State which parasite is depicted.
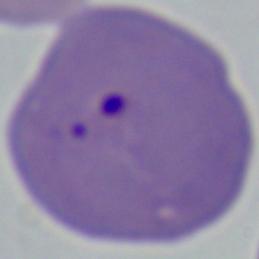

Babesia.

modality = micrograph
magnification = 1000x